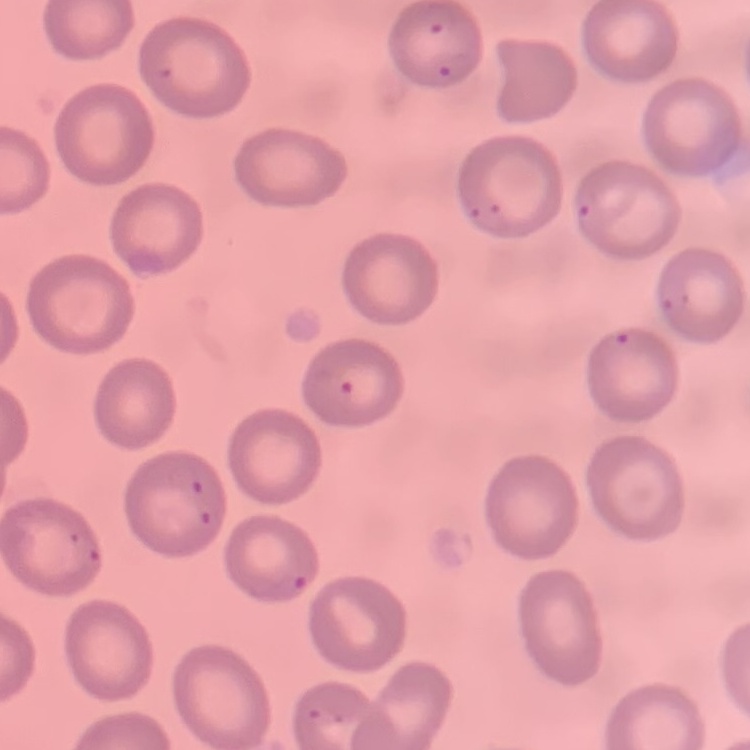 The erythrocytes show no rouleaux formation. Square crop of a larger photomicrograph. Field's or Giemsa stain. Thin blood smear.